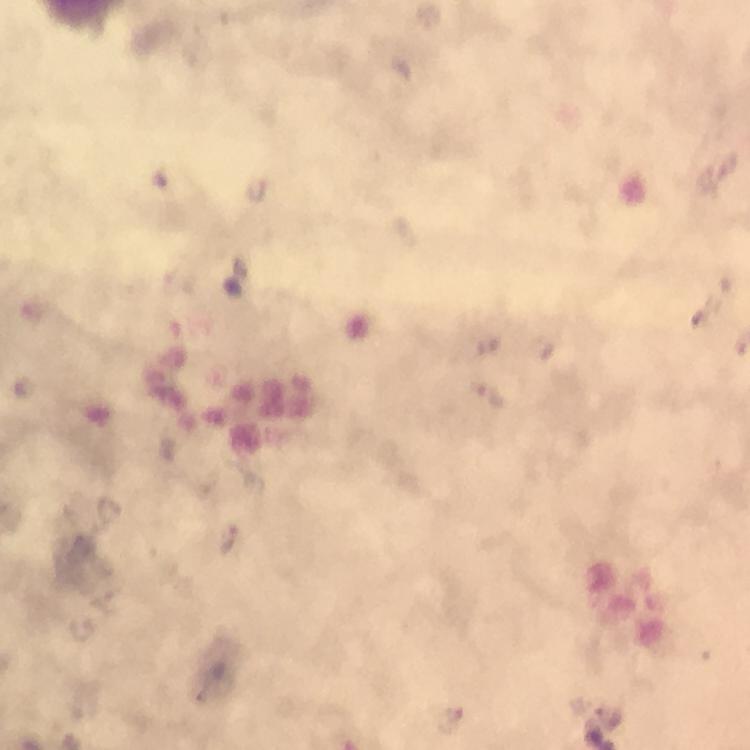

Approximate centers as {x, y} in pixels. Malaria parasite locations: {33, 310}, {22, 386}. A crop from one field of view. Immersion oil applied. Image is 750×750 pixels. At 100x magnification. Thick smear. From a malaria diagnostic workup. Giemsa-stained preparation. Photographed with a smartphone mounted on the microscope.